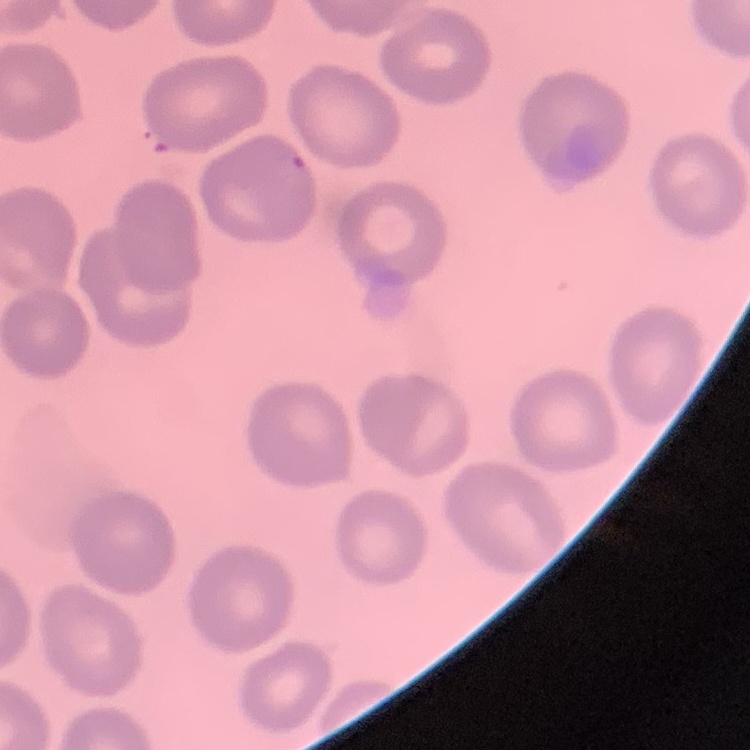

red blood cell morphology = no rouleaux formation
preparation = thin blood smear
image type = one tile cut from a larger photomicrograph
stain = Field's or Giemsa